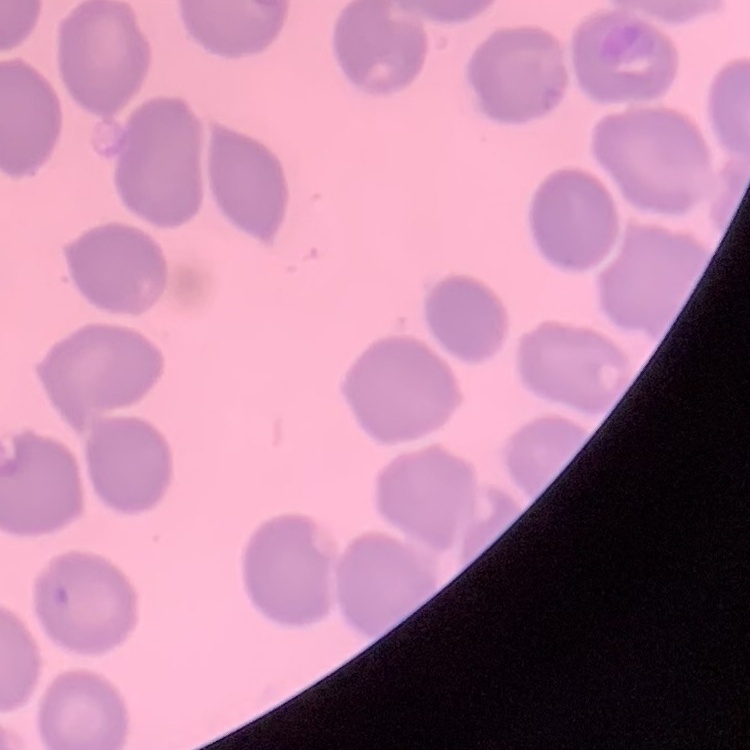

{
  "erythrocyte_morphology": "no rouleaux formation",
  "image_type": "square crop of a larger photomicrograph",
  "stain": "Field's or Giemsa",
  "preparation": "thin peripheral smear"
}